Describe the morphology of the red blood cells.
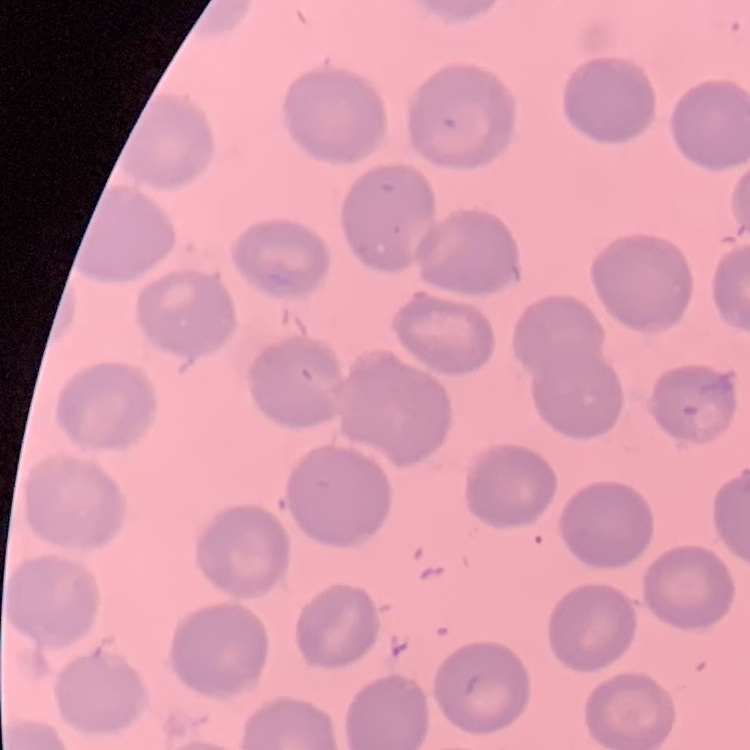
No rouleaux formation.

preparation = thin peripheral smear
image type = one tile cut from a larger photomicrograph
stain = Field's or Giemsa